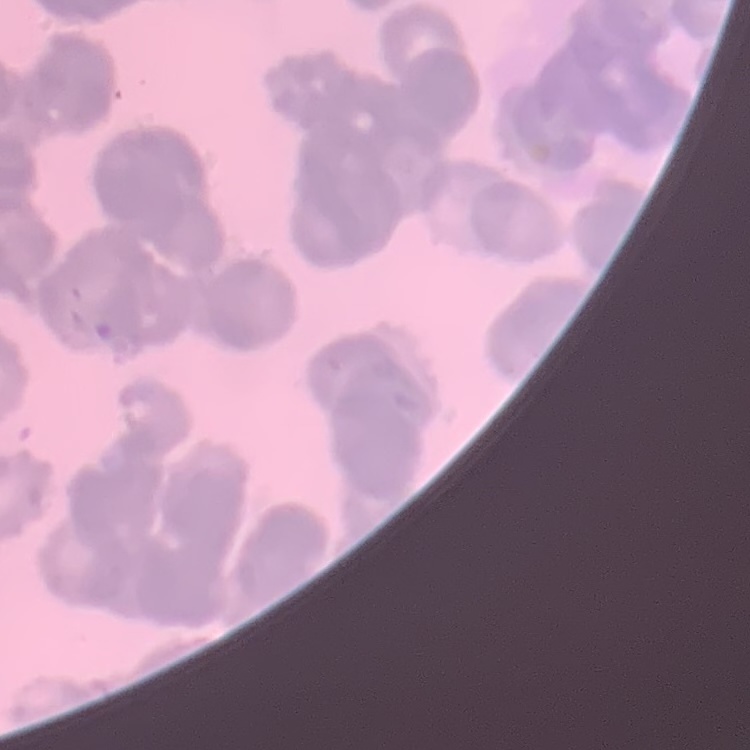

Summary:
  - Red blood cell morphology: rouleaux formation
  - Preparation: thin peripheral smear
  - Stain: Field's or Giemsa
  - Image type: one tile cut from a larger photomicrograph